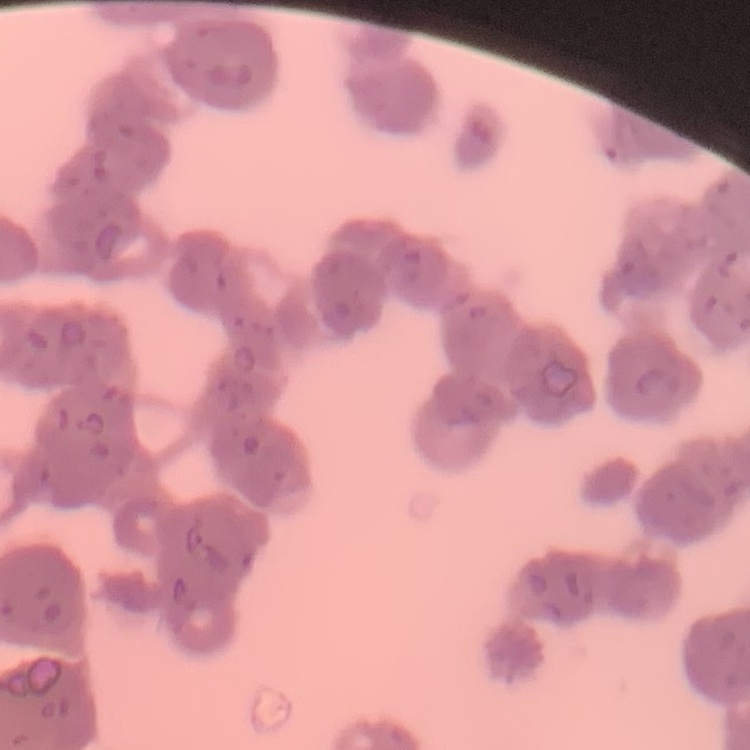 The red blood cells show rouleaux formation. Stained with either Field's or Giemsa. Thin peripheral smear. Square crop of a larger photomicrograph.